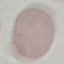
Malaria status: uninfected. Cell patch, automatically extracted from a larger field of view and resized to 64 × 64 pixels. Thin blood smear. Acquired by smartphone through the microscope eyepiece. Giemsa-stained preparation.